Report the malaria status.
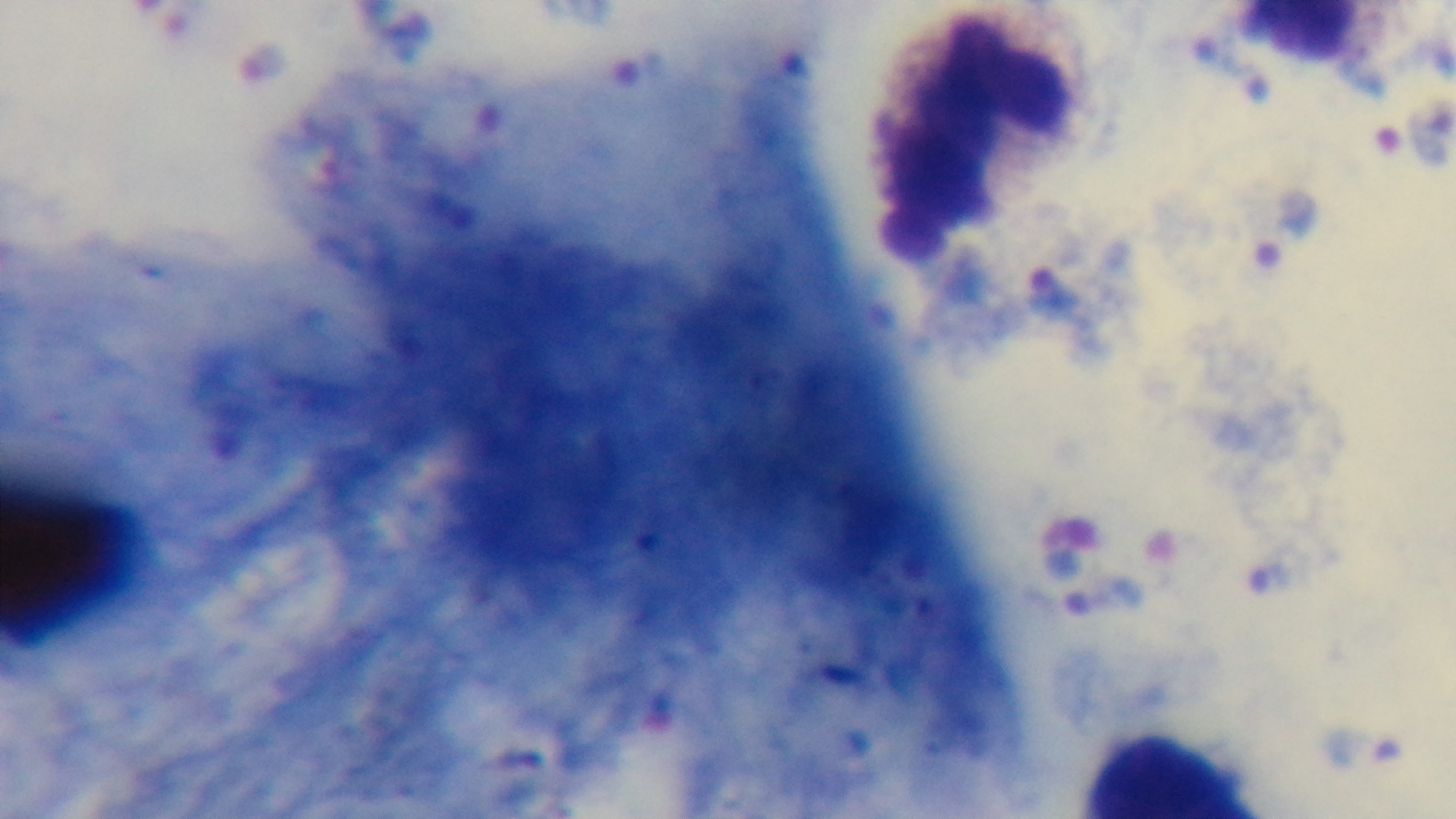
It is infected.

objective = 100x oil immersion
stain = Giemsa
field of view = one from the slide
preparation = thick
capture = mounted 4K digital camera
modality = light microscopy